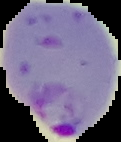
Image is 121×142 pixels. From a thin blood film. Malaria status: parasitized. Cell region segmented out of the field of view; the surrounding area is masked to black.